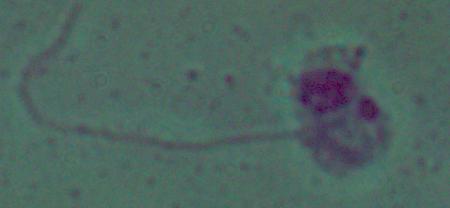
modality = micrograph
identification = Leishmania
magnification = 1000x